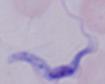

{
  "modality": "micrograph",
  "magnification": "1000x",
  "identification": "trypanosome"
}